Identify the parasite.
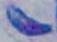

Toxoplasma gondii.

magnification = 1000x
modality = photomicrograph